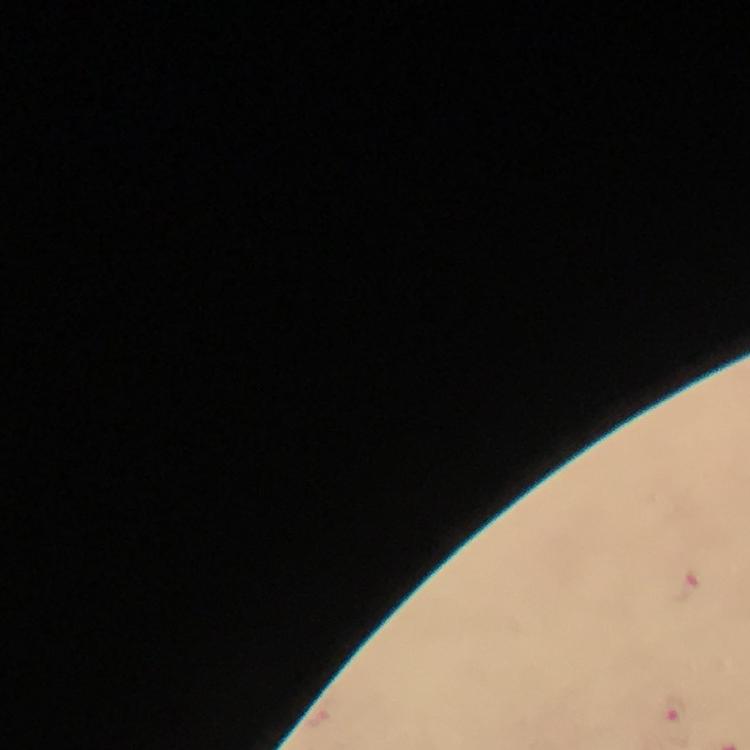
Approximate object centers, in pixels from the top-left corner. Plasmodium parasite locations: (x=684, y=586), (x=672, y=719). Giemsa stain. Cropped region of a single field of view. Immersion oil was used. Thick blood film. Photographed through the microscope with a smartphone camera. At 100x magnification. From a diagnostic examination for malaria. Image is 750×750 pixels.